Identify the cell.
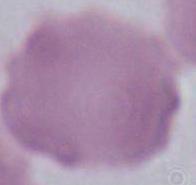
This is an erythrocyte.

magnification = 1000x
modality = photomicrograph